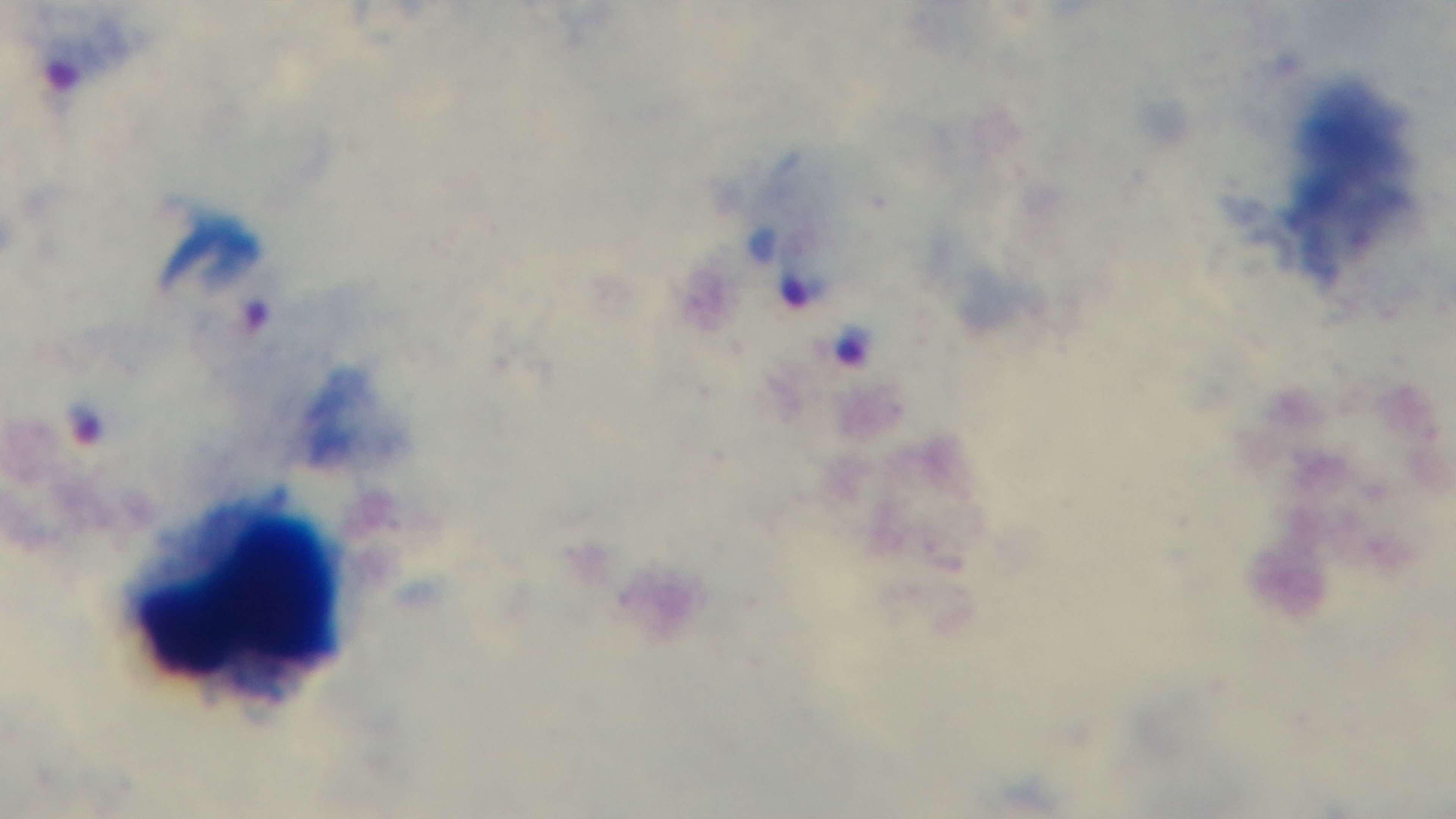
capture = mounted 4K digital camera
malaria status = positive
objective = 100x oil immersion
modality = light microscopy
preparation = thick smear
stain = Giemsa
field of view = one from the slide